Give the preparation type.
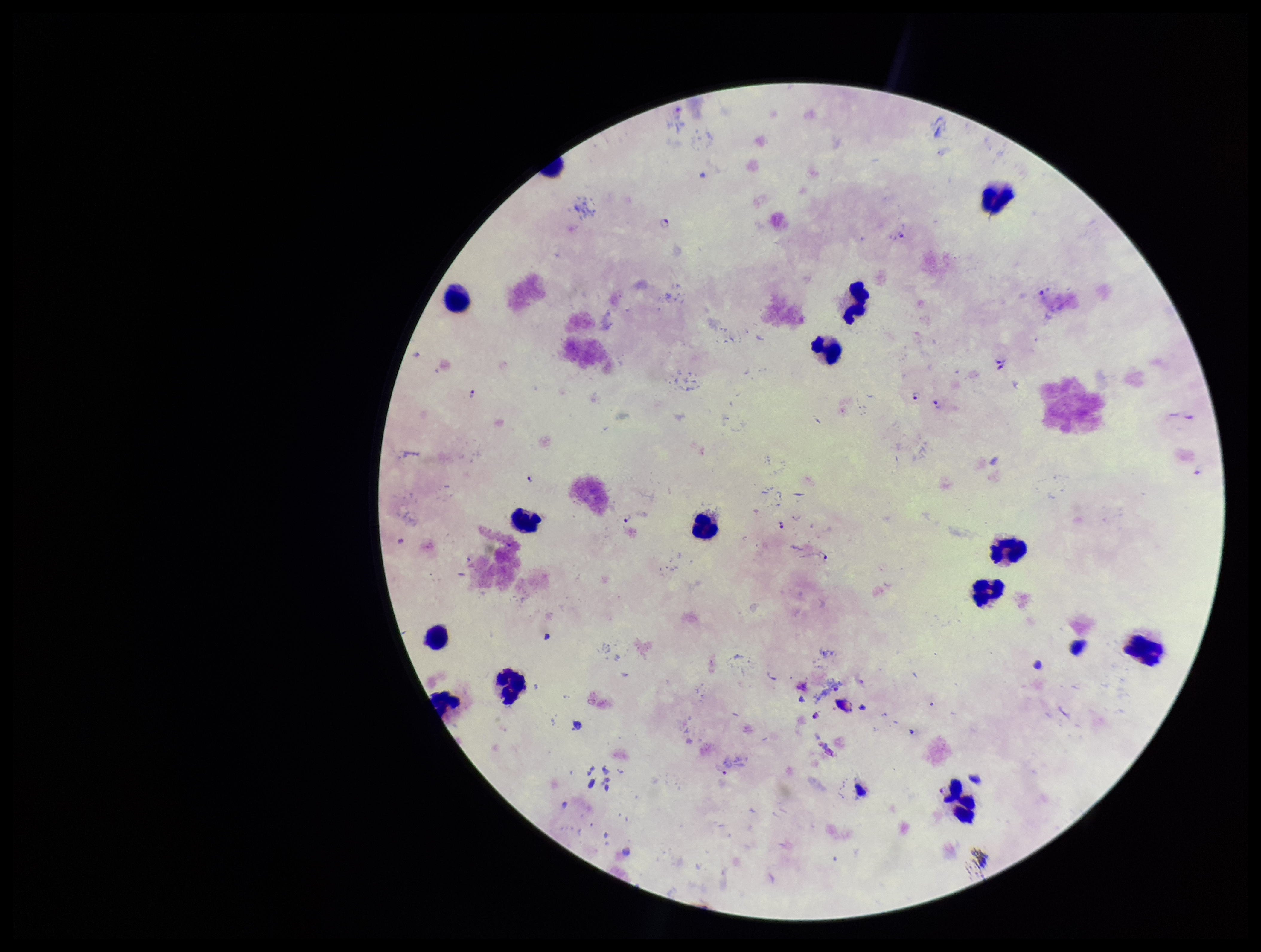

Thick.

Plasmodium parasites: seen. Leukocyte count: 14. Smartphone photograph taken through the eyepiece of a microscope. Single field of view. Species reported for this patient: Plasmodium falciparum. Parasite count: 12. Stained with Giemsa. Patient malaria status: positive. Image is 1261×952 pixels.